Report the malaria status of this cell.
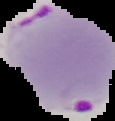

It is parasitized.

preparation = thin blood film
image type = segmented cell region on a black background
image size = 115×121 pixels